State the blood parasite species.
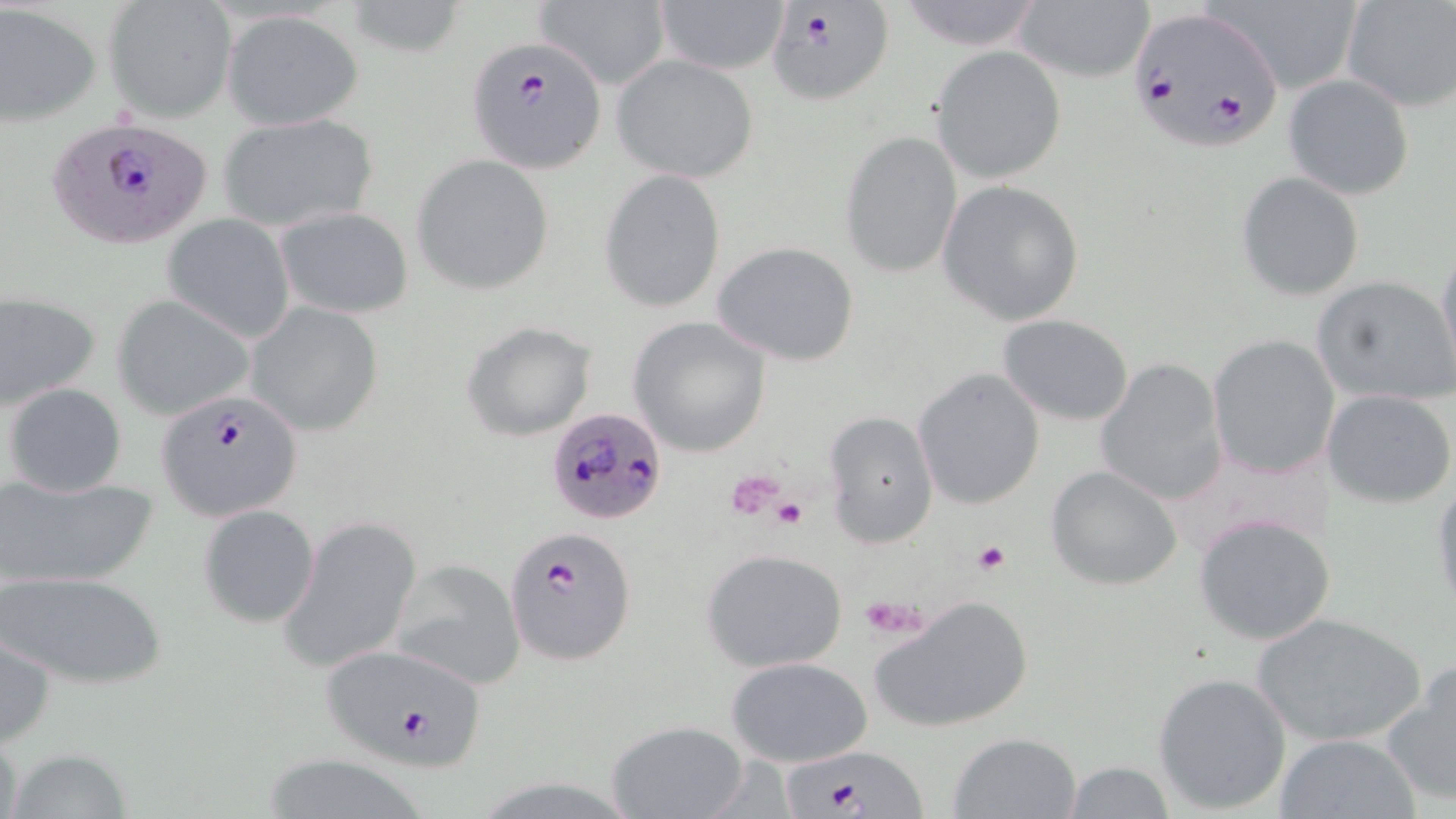
Plasmodium falciparum.

image size = 1456×819 pixels
modality = light microscopy
platelet locations = approximate bounding boxes as (x1,y1)-(x2,y2) corner pairs in pixels: (728,470)-(787,518), (770,497)-(807,529), (973,539)-(1010,577), (861,594)-(928,637)
preparation = thin blood smear
Plasmodium falciparum-infected red blood cell locations = approximate bounding boxes as (x1,y1)-(x2,y2) corner pairs in pixels: (766,4)-(895,108), (1128,6)-(1286,151), (465,36)-(607,172), (50,116)-(212,252), (156,389)-(303,522), (547,407)-(670,525), (507,528)-(637,664), (320,643)-(488,772), (785,747)-(924,818)
uninfected red blood cell locations = approximate bounding boxes as (x1,y1)-(x2,y2) corner pairs in pixels: (341,0)-(466,58), (533,0)-(671,89), (651,0)-(790,76), (891,0)-(1050,50), (1214,0)-(1368,99), (1340,0)-(1455,113), (103,1)-(235,123), (1012,1)-(1156,86), (0,4)-(100,127), (222,11)-(364,130), (931,45)-(1067,185), (611,53)-(759,183), (1284,74)-(1414,200), (217,112)-(378,234), (839,131)-(962,279), (412,156)-(553,292), (598,169)-(727,313), (1236,172)-(1365,301), (937,180)-(1085,325), (276,206)-(413,319), (161,215)-(295,343), (712,240)-(861,367), (1436,240)-(1456,385), (1312,275)-(1456,407), (0,289)-(101,411), (114,294)-(255,422), (247,302)-(384,438), (997,314)-(1136,424), (628,317)-(773,456), (461,320)-(598,441), (1207,333)-(1341,479), (1094,357)-(1228,506), (912,367)-(1044,509), (4,382)-(127,496), (1323,387)-(1455,508), (824,410)-(938,550), (1046,464)-(1185,590), (0,471)-(157,591), (1430,477)-(1456,617), (198,505)-(320,629), (1194,515)-(1335,645), (279,516)-(422,675), (701,548)-(847,672), (390,559)-(526,690), (1,569)-(169,691), (869,594)-(1035,735), (1250,613)-(1426,747), (1,630)-(56,749), (726,656)-(875,769), (1381,662)-(1456,809), (1152,671)-(1293,815), (605,719)-(750,819), (946,731)-(1082,818), (1274,732)-(1420,818), (1,733)-(26,819), (5,747)-(136,819), (256,753)-(439,818), (1059,761)-(1178,817)
field of view = one of a larger specimen
magnification = 1000x
stain = May-Grünwald-Giemsa